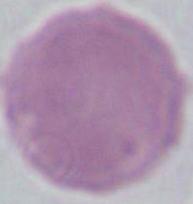
{
  "magnification": "1000x",
  "modality": "photomicrograph",
  "identification": "erythrocyte"
}